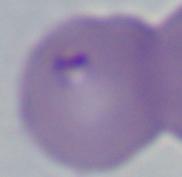
{
  "identification": "Babesia",
  "magnification": "1000x",
  "modality": "photomicrograph"
}